Classify this cell by malaria status.
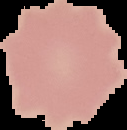
It is uninfected.

Summary:
  - Image size: 127×130 pixels
  - Preparation: thin blood film
  - Image type: cell region segmented out of the field of view; surrounding area masked to black